Assess this cell for malaria.
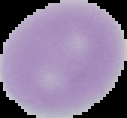

It is uninfected.

From a thin blood smear. Cell region segmented out of the field of view; the surrounding area is masked to black. Image is 127×118 pixels.